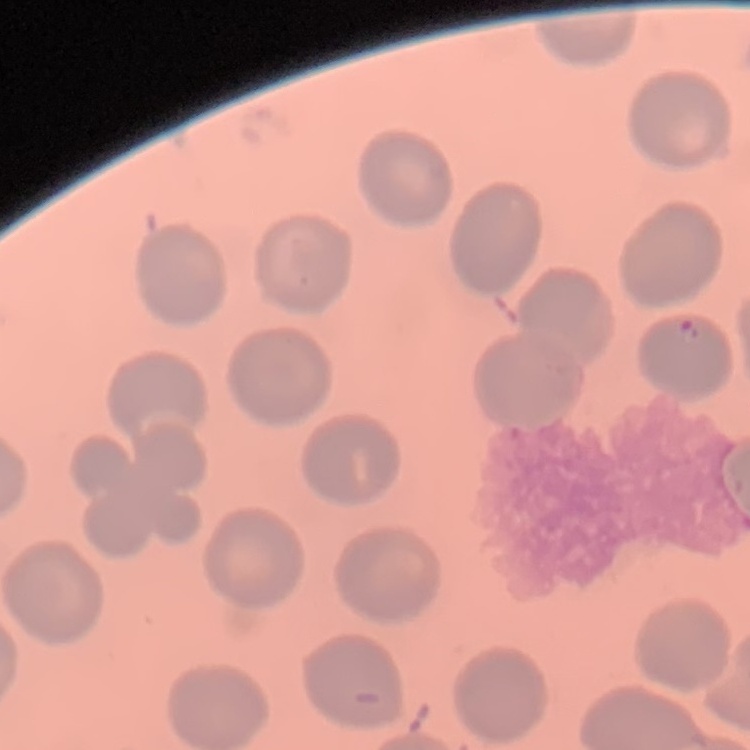
{
  "erythrocyte_morphology": "no rouleaux formation",
  "image_type": "square crop of a larger photomicrograph",
  "preparation": "thin peripheral smear",
  "stain": "Field's or Giemsa"
}